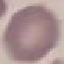

Result: no malaria parasites seen. Acquired by smartphone through the microscope eyepiece. Giemsa stain. Automatically extracted cell patch, resized to 64 × 64 pixels. Thin smear of blood.